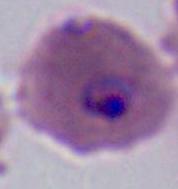
magnification = 400x or 1000x
modality = photomicrograph
identification = Plasmodium